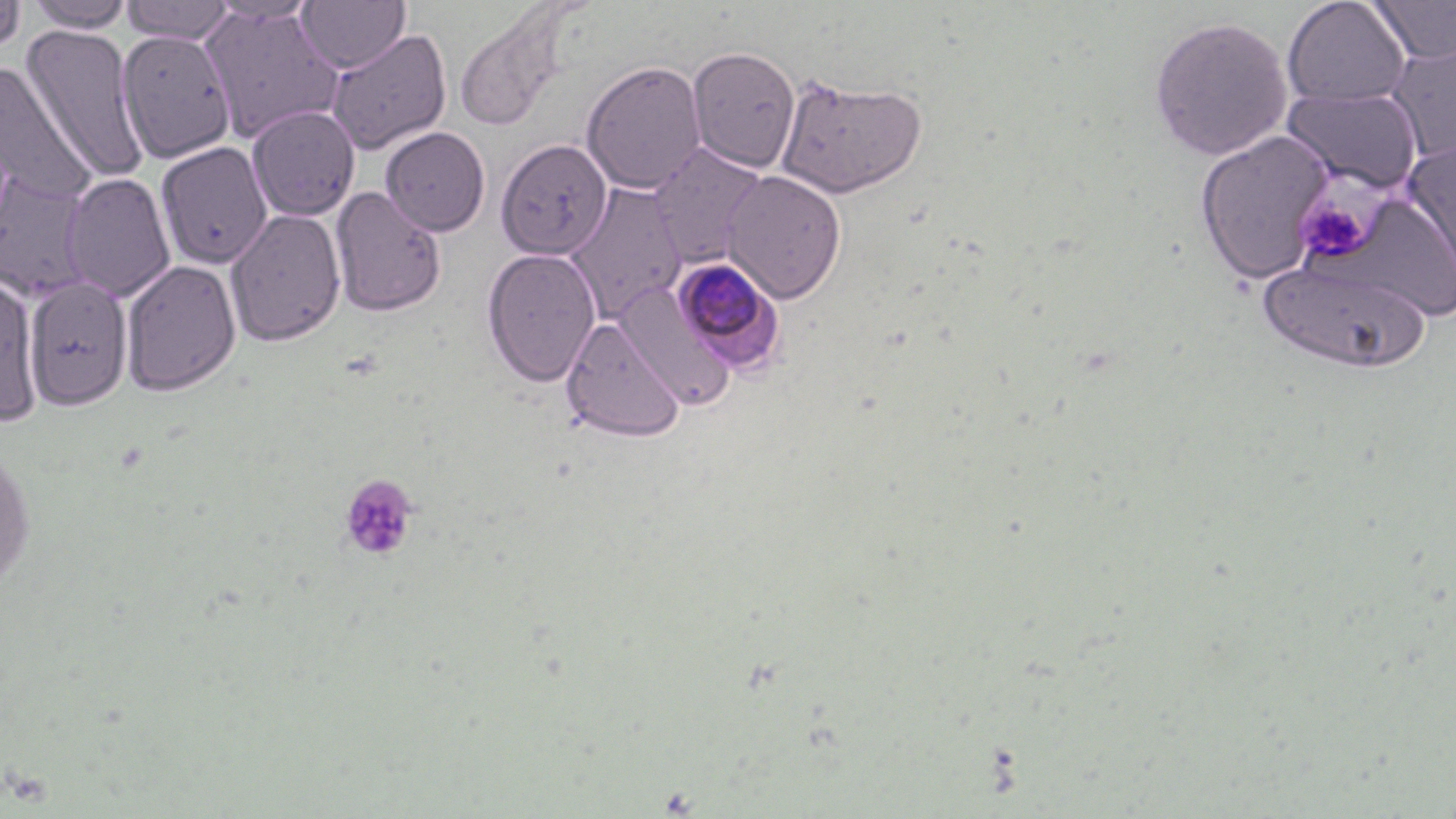

Summary:
  - Coordinate format: approximate bounding boxes as [x1, y1, x2, y2] in pixels
  - Plasmodium malariae-infected red blood cell locations: [673, 255, 786, 374]
  - Platelet locations: [1293, 189, 1379, 268], [338, 473, 419, 561]
  - Uninfected red blood cell locations: [0, 0, 26, 58], [122, 0, 236, 43], [296, 0, 409, 73], [1282, 0, 1411, 109], [1367, 0, 1456, 64], [26, 1, 134, 32], [200, 4, 343, 144], [454, 8, 565, 134], [1149, 16, 1292, 161], [21, 24, 148, 182], [116, 28, 236, 163], [326, 28, 452, 155], [1385, 42, 1456, 163], [687, 45, 800, 173], [0, 59, 96, 203], [582, 60, 707, 194], [776, 74, 927, 198], [1282, 86, 1423, 194], [247, 105, 360, 221], [380, 127, 490, 236], [1194, 130, 1333, 285], [496, 138, 612, 259], [1402, 140, 1456, 290], [155, 142, 273, 269], [649, 144, 769, 265], [722, 170, 847, 303], [1, 172, 93, 301], [61, 172, 176, 302], [566, 184, 687, 323], [330, 186, 447, 317], [225, 208, 347, 347], [481, 248, 602, 387], [1258, 258, 1429, 373], [121, 259, 241, 396], [0, 274, 42, 426], [25, 277, 133, 409], [612, 280, 735, 409], [560, 316, 686, 442], [0, 444, 36, 595]
  - Slide-level diagnosis: Plasmodium malariae
  - Preparation: thin blood smear
  - Stain: May-Grünwald-Giemsa
  - Modality: light microscopy
  - Field of view: one of a larger specimen
  - Magnification: 1000x
  - Image size: 1456×819 pixels